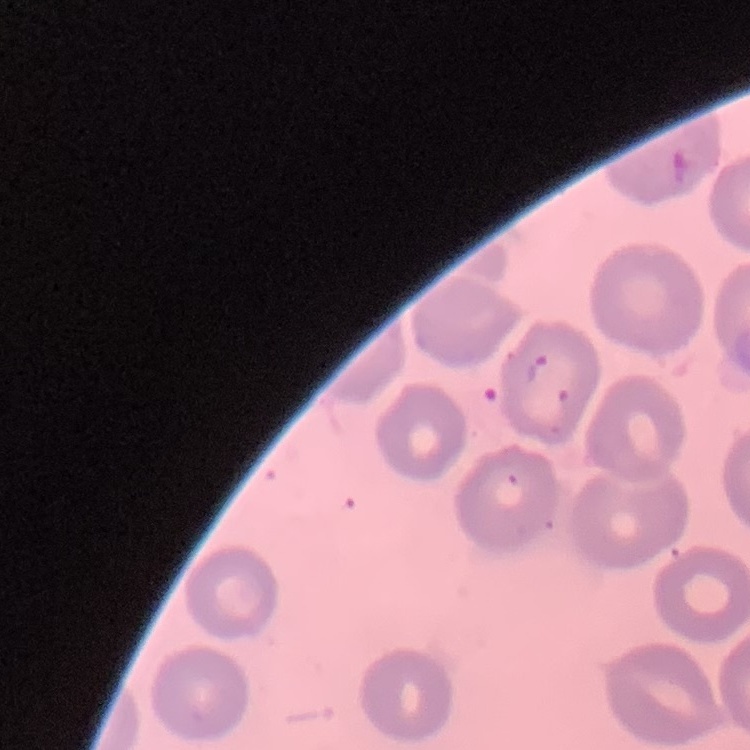

Summary:
  - Red blood cell morphology: no rouleaux formation
  - Stain: Field's or Giemsa
  - Preparation: thin peripheral smear
  - Image type: one tile cut from a larger photomicrograph